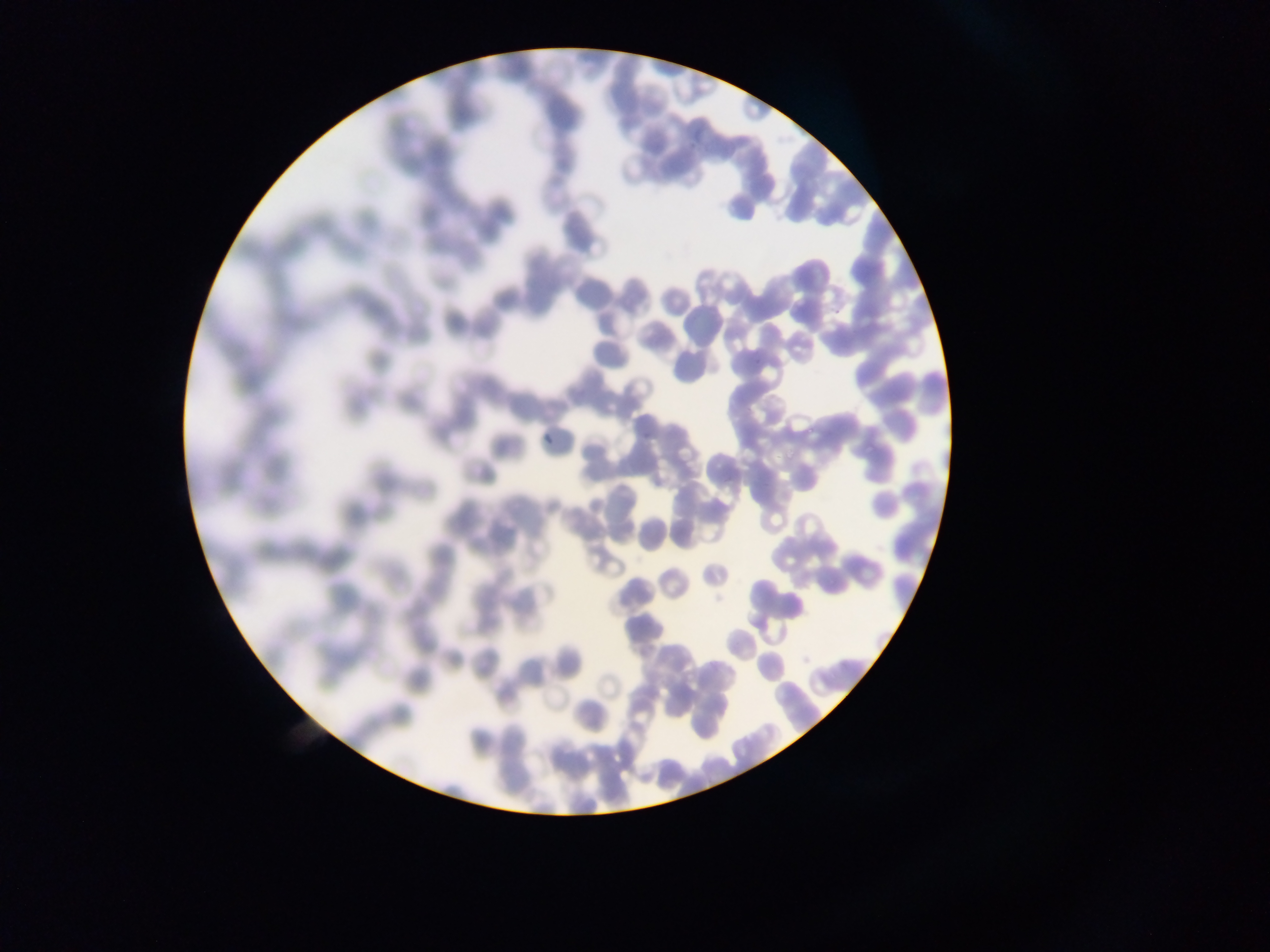

Approximate bounding boxes as [left, top, right, bottom] in pixels.
Summary:
  - Malaria parasite locations: [805, 418, 819, 436], [862, 442, 878, 459], [779, 443, 802, 465]
  - Field of view: single
  - Capture: mobile-phone photograph through a microscope
  - Image size: 1270×952 pixels
  - Country: Ghana
  - Preparation: thin blood film